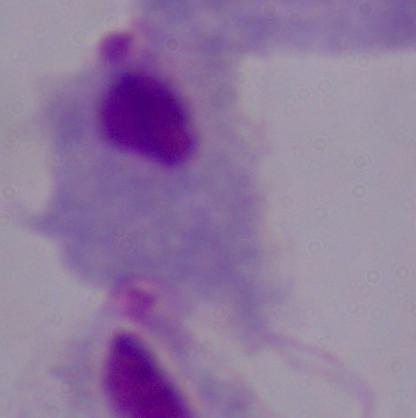 Captured at 1000x magnification. A trichomonad is seen. Micrograph.